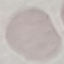

Summary:
  - Result: no malaria parasites detected
  - Stain: Giemsa
  - Preparation: thin blood smear
  - Image type: automatically extracted cell patch, resized to 64 × 64 pixels
  - Capture: smartphone camera at the microscope eyepiece